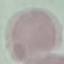
Summary:
  - Result: no malaria parasites seen
  - Image type: automatically extracted cell patch, resized to 64 × 64 pixels
  - Stain: Giemsa
  - Capture: smartphone camera at the microscope eyepiece
  - Preparation: thin blood smear